Outline each blood parasite and name the species.
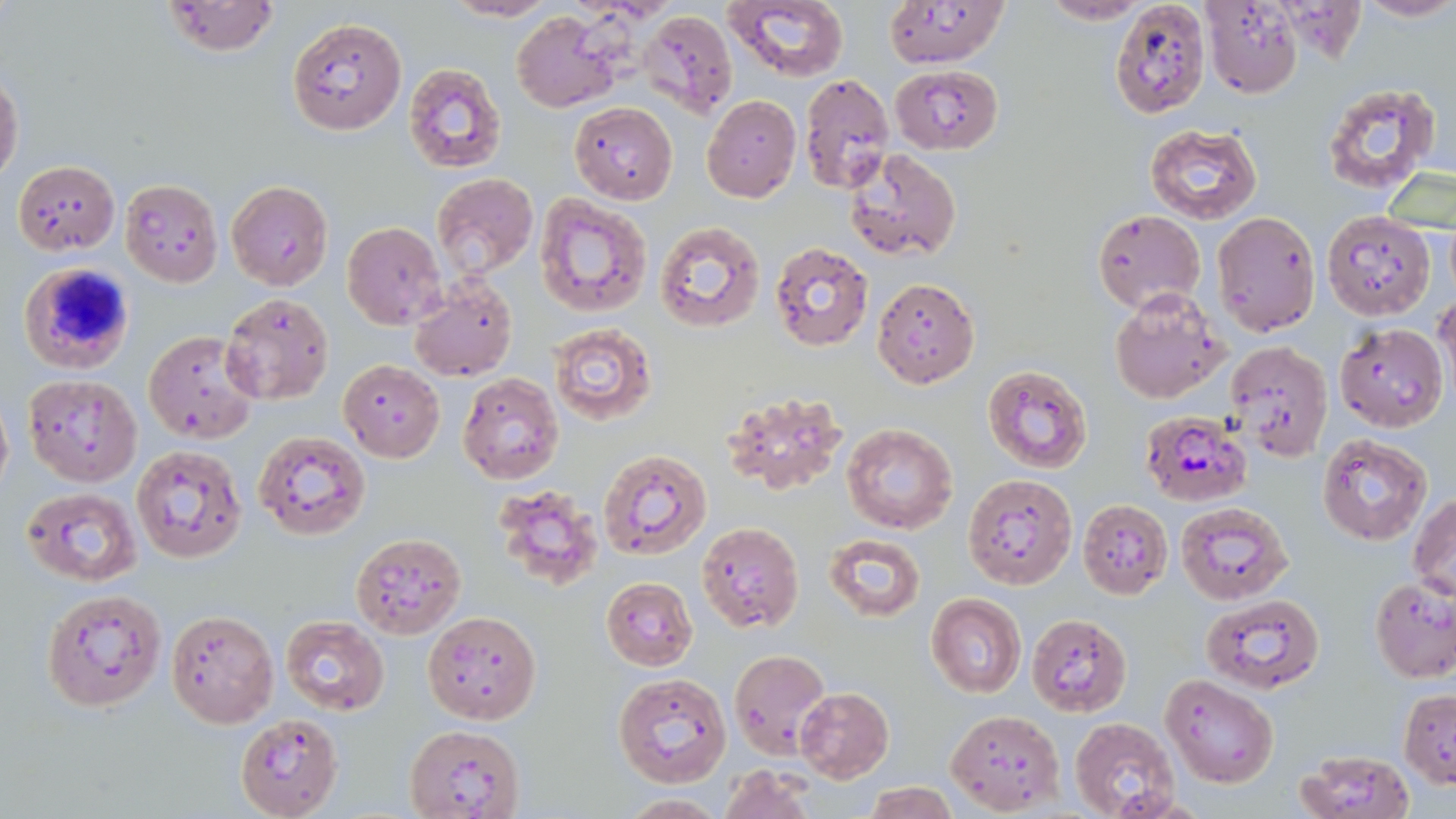
Approximate bounding boxes as (x1,y1)-(x2,y2) corner pairs in pixels.
Plasmodium falciparum-infected red blood cells: (1138,409)-(1253,507).
No Plasmodium ovale, Plasmodium malariae, Plasmodium vivax, Babesia divergens, or Trypanosoma brucei observed.

Uninfected red blood cell locations: (442,0)-(559,23), (881,0)-(1009,69), (161,1)-(280,57), (725,1)-(850,82), (1038,1)-(1156,25), (1200,1)-(1305,97), (1351,1)-(1456,25), (1109,2)-(1210,118), (640,9)-(739,117), (512,10)-(620,113), (288,15)-(407,136), (403,63)-(506,172), (891,65)-(1003,154), (799,74)-(894,194), (0,75)-(24,187), (1321,82)-(1442,195), (701,94)-(801,203), (569,101)-(677,204), (1145,124)-(1261,224), (845,148)-(962,262), (12,161)-(119,254), (431,174)-(539,281), (119,178)-(222,286), (227,180)-(333,290), (535,193)-(652,316), (1321,210)-(1435,320), (1093,211)-(1205,312), (1212,212)-(1321,336), (653,220)-(767,334), (342,221)-(446,328), (769,241)-(874,351), (18,261)-(136,374), (872,278)-(979,388), (409,279)-(517,383), (1110,288)-(1232,404), (1435,290)-(1456,398), (220,292)-(335,407), (1335,322)-(1448,431), (547,323)-(657,425), (144,329)-(258,443), (1225,340)-(1333,459), (338,359)-(445,462), (984,363)-(1094,475), (458,373)-(564,485), (23,374)-(142,488), (0,391)-(13,497), (720,392)-(849,496), (843,423)-(958,532), (254,430)-(371,540), (1318,433)-(1433,546), (131,445)-(248,565), (598,448)-(712,561), (962,473)-(1078,588), (498,485)-(608,593), (22,486)-(141,585), (1410,493)-(1456,601), (1077,499)-(1173,599), (1174,500)-(1292,604), (697,520)-(805,633), (351,531)-(466,637), (823,533)-(925,622), (601,577)-(696,670), (1370,577)-(1456,682), (42,589)-(167,712), (926,593)-(1027,697), (1202,593)-(1325,691), (166,608)-(279,727), (423,611)-(541,724), (1026,614)-(1132,716), (280,616)-(391,714), (728,649)-(831,756), (613,673)-(732,788), (1161,675)-(1280,788), (793,687)-(894,781), (1399,690)-(1456,787), (946,709)-(1064,813), (234,712)-(342,819), (1068,716)-(1181,819), (404,724)-(527,818), (1293,751)-(1416,819), (717,765)-(817,819), (862,782)-(960,819), (619,794)-(730,817). Slide-level diagnosis: Plasmodium falciparum. Light microscopy. May-Grünwald-Giemsa-stained preparation. One field of a larger specimen. 1000x magnification. Thin blood smear. Image is 1456×819 pixels.